Outline each blood parasite and name the species.
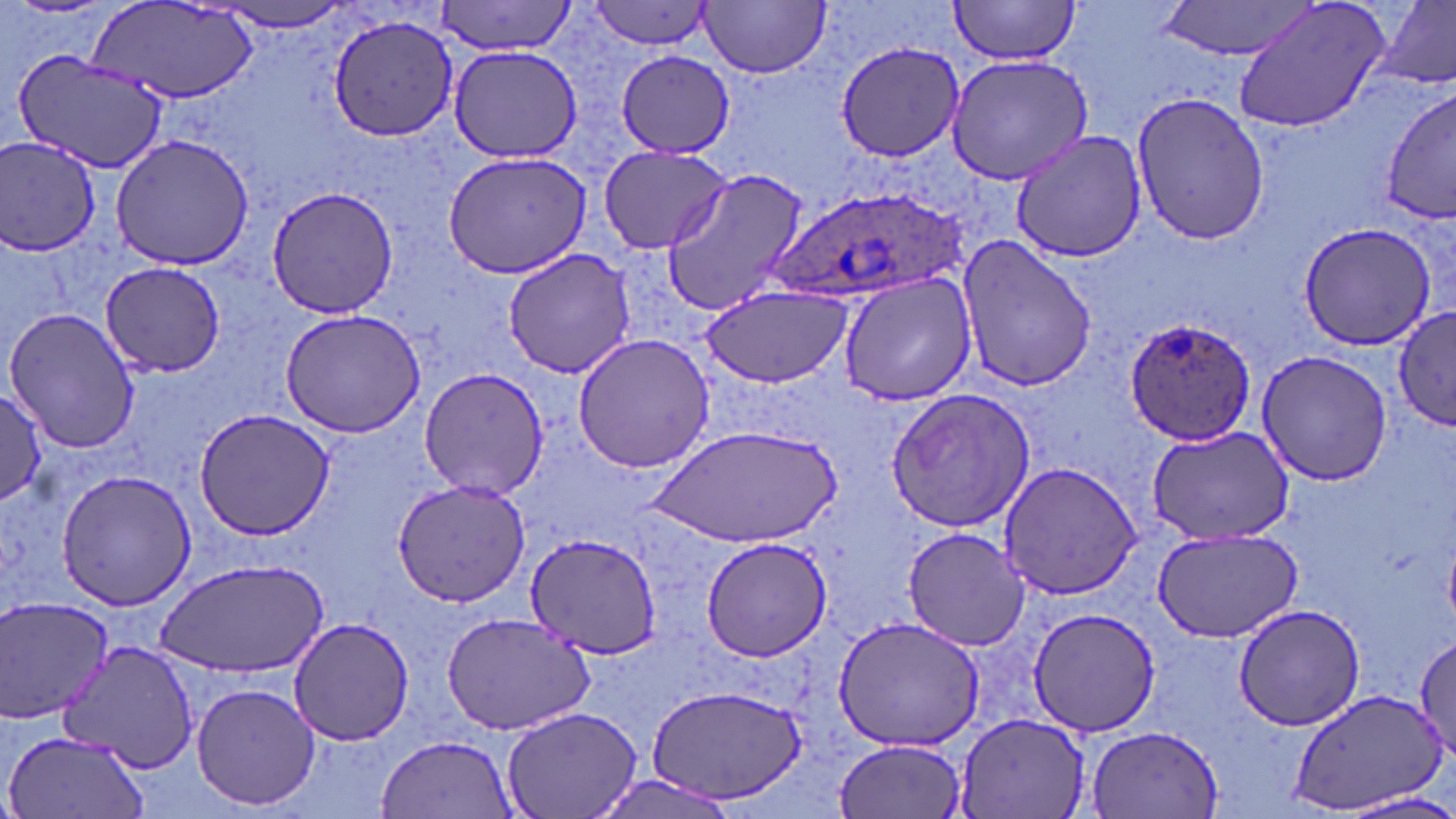
Approximate bounding boxes as (x1,y1)-(x2,y2) corner pairs in pixels.
Plasmodium ovale-infected red blood cells: (773,184)-(968,307), (1124,315)-(1261,447).
No Plasmodium falciparum, Plasmodium malariae, Plasmodium vivax, Babesia divergens, or Trypanosoma brucei observed.

{
  "slide_level_diagnosis": "Plasmodium ovale",
  "magnification": "1000x",
  "field_of_view": "single",
  "image_size": "1456×819 pixels",
  "stain": "May-Grünwald-Giemsa",
  "preparation": "thin blood smear",
  "modality": "optical microscopy",
  "uninfected_red_blood_cell_locations": "approximate bounding boxes as (x1,y1)-(x2,y2) corner pairs in pixels: (947,0)-(1083,66), (1155,0)-(1323,60), (1229,0)-(1392,135), (1377,0)-(1456,90), (206,1)-(364,33), (431,1)-(578,58), (700,1)-(830,78), (90,2)-(263,104), (583,2)-(718,52), (329,15)-(460,141), (835,40)-(964,164), (445,45)-(586,163), (615,49)-(735,159), (13,50)-(171,172), (944,54)-(1097,187), (1381,84)-(1456,227), (1130,89)-(1269,245), (1011,132)-(1146,264), (110,133)-(256,271), (0,136)-(103,256), (598,145)-(736,256), (441,150)-(593,280), (660,166)-(811,316), (268,185)-(399,319), (1298,221)-(1440,352), (956,235)-(1098,392), (500,248)-(639,378), (99,261)-(229,375), (838,272)-(978,405), (698,284)-(853,390), (1394,306)-(1455,430), (4,307)-(140,454), (278,308)-(428,438), (573,333)-(718,475), (1255,349)-(1394,486), (418,368)-(549,498), (884,385)-(1036,533), (0,393)-(48,506), (194,410)-(336,540), (649,425)-(843,549), (1144,426)-(1295,545), (999,462)-(1142,599), (54,470)-(198,611), (391,478)-(531,608), (901,526)-(1033,651), (1151,526)-(1303,642), (523,533)-(663,659), (700,536)-(835,663), (158,560)-(326,675), (0,595)-(115,722), (1229,603)-(1368,733), (1027,607)-(1163,736), (442,611)-(596,736), (832,615)-(986,753), (288,616)-(413,747), (1415,629)-(1456,765), (59,640)-(199,773), (189,681)-(323,814), (645,685)-(808,806), (1287,687)-(1446,815), (503,707)-(641,819), (953,714)-(1094,819), (1083,723)-(1226,817), (4,729)-(151,819), (377,735)-(520,818), (835,737)-(967,819), (590,772)-(745,818), (1334,791)-(1456,819)"
}